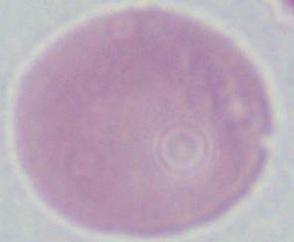

{
  "magnification": "1000x",
  "identification": "red blood cell",
  "modality": "micrograph"
}